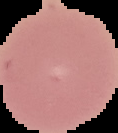 Result: negative for Plasmodium parasites. The area outside the segmented cell region is set to black. Image is 118×133 pixels. From a thin blood film.